Mark where platelets are.
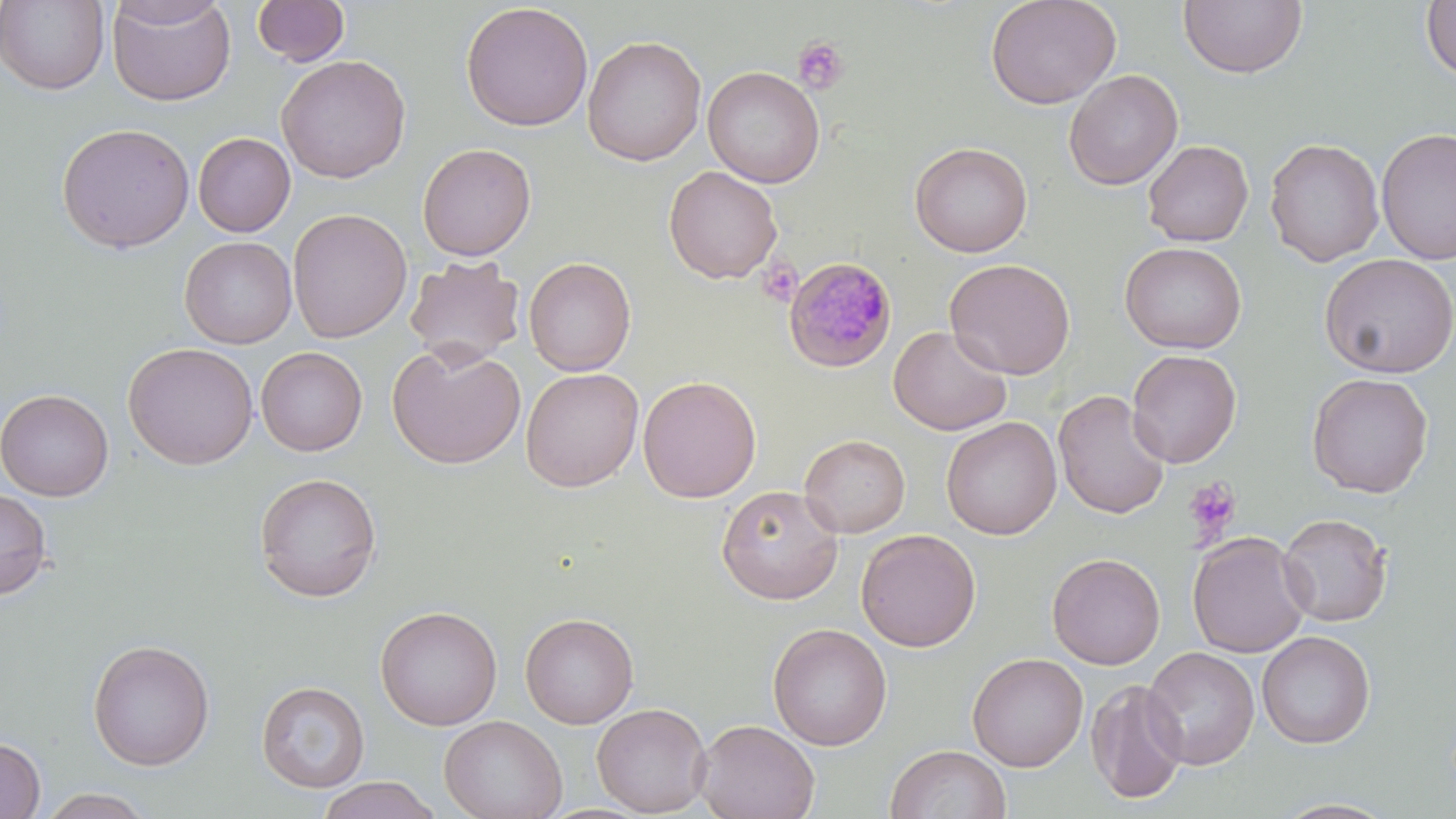

Approximate bounding boxes as [x1, y1, x2, y2] in pixels.
Platelets: [792, 37, 850, 95], [757, 259, 801, 307], [1182, 477, 1241, 546].

Summary:
  - Plasmodium malariae-infected red blood cell locations: [783, 257, 899, 374]
  - Uninfected red blood cell locations: [106, 0, 236, 107], [108, 0, 230, 28], [252, 0, 351, 66], [985, 0, 1121, 110], [0, 1, 110, 95], [1178, 1, 1308, 79], [1421, 1, 1455, 83], [460, 2, 594, 132], [582, 34, 707, 167], [276, 54, 411, 184], [703, 66, 825, 188], [1063, 69, 1183, 190], [56, 122, 195, 253], [1376, 126, 1456, 266], [193, 132, 295, 237], [1264, 137, 1384, 267], [1142, 140, 1254, 247], [909, 141, 1033, 258], [417, 143, 537, 261], [663, 166, 783, 284], [287, 208, 412, 343], [179, 236, 297, 349], [1119, 241, 1247, 354], [1319, 253, 1456, 378], [404, 255, 526, 367], [522, 256, 637, 377], [944, 258, 1076, 379], [888, 324, 1013, 436], [387, 341, 526, 469], [123, 342, 258, 470], [256, 347, 368, 456], [1126, 349, 1242, 468], [521, 368, 643, 491], [1306, 372, 1434, 498], [637, 375, 761, 503], [1, 388, 113, 501], [1052, 390, 1171, 520], [941, 416, 1062, 540], [799, 434, 910, 538], [253, 472, 382, 602], [0, 485, 53, 600], [716, 485, 843, 605], [1277, 513, 1393, 627], [856, 528, 981, 652], [1187, 532, 1312, 658], [1047, 552, 1166, 670], [375, 605, 502, 730], [520, 612, 638, 728], [768, 622, 892, 750], [1257, 630, 1375, 749], [87, 638, 215, 770], [1141, 646, 1260, 770], [967, 652, 1088, 771], [1085, 678, 1189, 803], [256, 680, 370, 793], [592, 702, 712, 816], [439, 714, 567, 819], [694, 718, 820, 819], [0, 737, 46, 818], [885, 744, 1011, 819], [316, 776, 441, 819], [36, 787, 156, 818], [1270, 797, 1400, 818]
  - Slide-level diagnosis: Plasmodium malariae
  - Preparation: thin blood film
  - Modality: light microscopy
  - Field of view: one of a larger specimen
  - Image size: 1456×819 pixels
  - Stain: May-Grünwald-Giemsa
  - Magnification: 1000x